Name the blood parasite species.
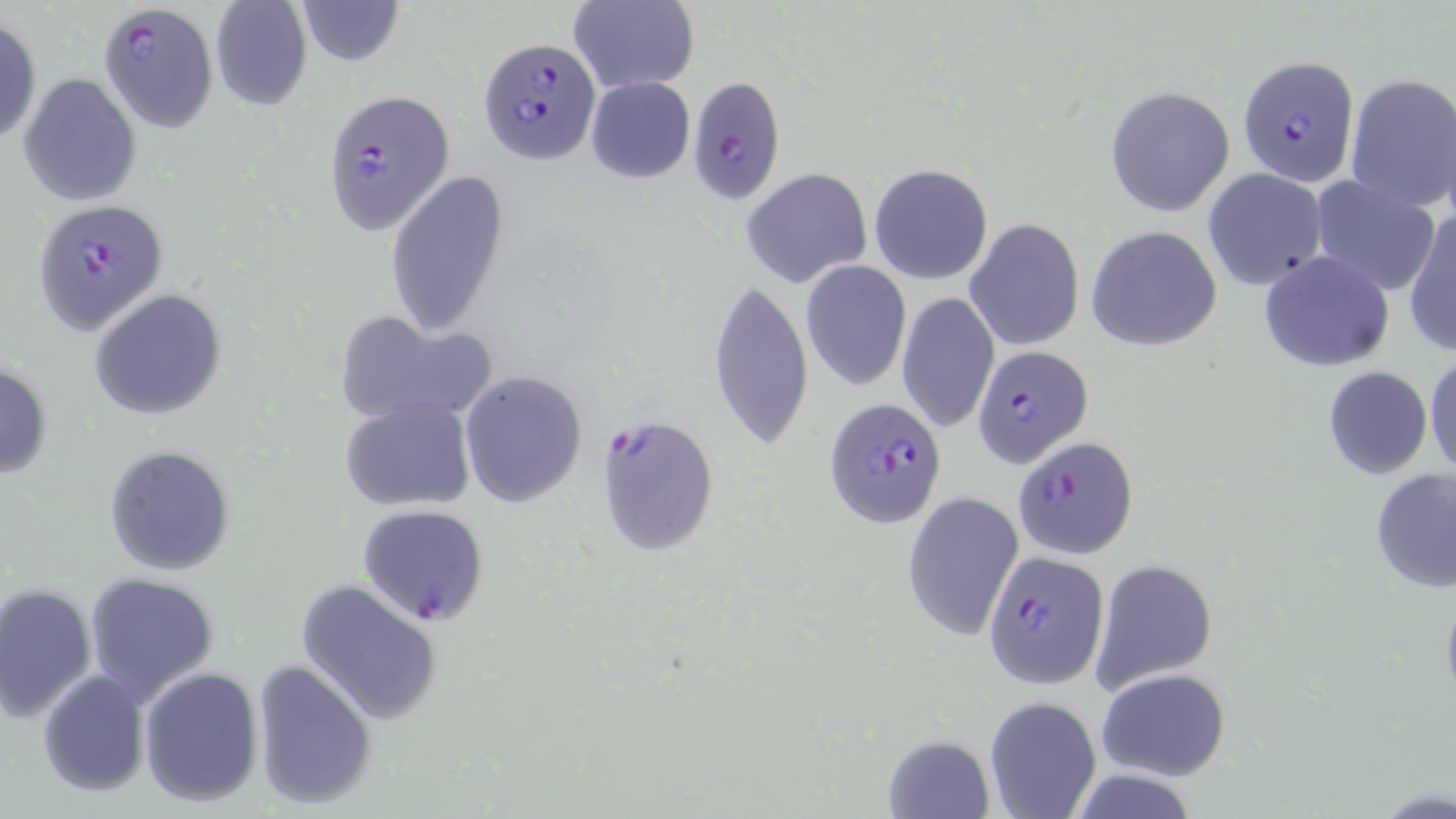

Plasmodium falciparum.

Summary:
  - Coordinate format: approximate bounding boxes as [x1, y1, x2, y2] in pixels
  - Plasmodium falciparum-infected red blood cell locations: [97, 4, 217, 132], [477, 37, 602, 167], [1237, 54, 1363, 189], [675, 77, 788, 202], [322, 89, 455, 235], [32, 200, 165, 334], [971, 344, 1094, 467], [824, 396, 946, 530], [595, 414, 719, 557], [1013, 435, 1140, 560], [357, 502, 489, 627], [983, 549, 1108, 691]
  - Uninfected red blood cell locations: [294, 0, 404, 65], [568, 0, 698, 94], [209, 1, 313, 112], [0, 16, 42, 150], [18, 72, 141, 207], [1343, 72, 1456, 216], [584, 75, 696, 184], [1104, 85, 1235, 216], [869, 164, 994, 286], [741, 167, 872, 288], [1202, 167, 1327, 290], [383, 169, 509, 335], [1308, 175, 1440, 295], [1280, 202, 1420, 349], [1406, 207, 1455, 357], [964, 219, 1085, 352], [1086, 225, 1222, 351], [1258, 248, 1395, 372], [800, 261, 912, 391], [706, 279, 809, 450], [897, 289, 1000, 435], [88, 290, 225, 419], [332, 311, 494, 427], [1424, 349, 1456, 482], [0, 359, 52, 483], [1321, 366, 1433, 481], [458, 370, 587, 507], [339, 398, 476, 514], [103, 444, 236, 576], [1369, 468, 1456, 594], [901, 490, 1024, 642], [1092, 558, 1219, 693], [83, 572, 221, 704], [295, 577, 444, 725], [1, 583, 98, 722], [251, 657, 378, 810], [139, 666, 264, 808], [1096, 667, 1233, 781], [37, 670, 150, 797], [983, 694, 1102, 819], [884, 732, 994, 818]
  - Magnification: 1000x
  - Preparation: thin blood film
  - Image size: 1456×819 pixels
  - Modality: light microscopy
  - Stain: May-Grünwald-Giemsa
  - Field of view: single